Locate white blood cells.
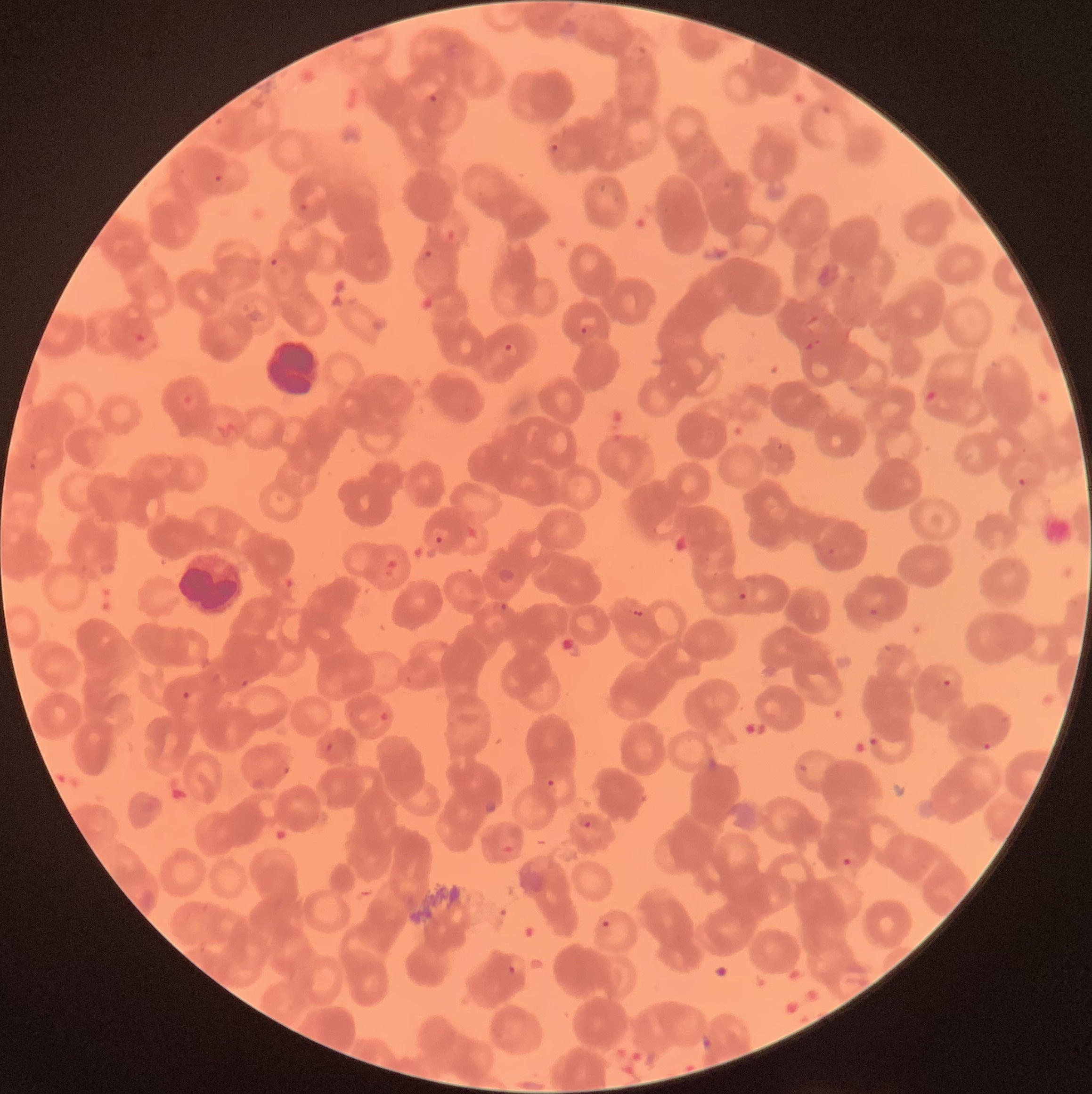
Approximate bounding boxes as named x1/y1/x2/y2 corners in pixels.
White blood cells: (x1=268, y1=337, x2=318, y2=396), (x1=180, y1=552, x2=242, y2=612).

Summary:
  - Plasmodium parasite locations: (x1=425, y1=93, x2=438, y2=103), (x1=549, y1=142, x2=562, y2=160), (x1=214, y1=174, x2=223, y2=182), (x1=298, y1=203, x2=309, y2=214), (x1=423, y1=249, x2=434, y2=258), (x1=269, y1=258, x2=278, y2=266), (x1=581, y1=326, x2=589, y2=335), (x1=504, y1=341, x2=519, y2=355), (x1=30, y1=453, x2=38, y2=472), (x1=1018, y1=478, x2=1026, y2=486), (x1=431, y1=526, x2=449, y2=544), (x1=826, y1=548, x2=835, y2=555), (x1=737, y1=592, x2=748, y2=601), (x1=493, y1=602, x2=509, y2=615), (x1=868, y1=608, x2=879, y2=617), (x1=882, y1=643, x2=892, y2=653), (x1=940, y1=678, x2=952, y2=689), (x1=868, y1=737, x2=878, y2=747), (x1=982, y1=742, x2=992, y2=749), (x1=797, y1=763, x2=808, y2=773), (x1=547, y1=779, x2=555, y2=788), (x1=484, y1=802, x2=497, y2=814), (x1=576, y1=812, x2=596, y2=828), (x1=841, y1=857, x2=852, y2=866), (x1=601, y1=920, x2=610, y2=928), (x1=505, y1=964, x2=519, y2=974)
  - Preparation: thin blood film
  - Red blood cell morphology: rouleaux formation
  - Modality: light microscopy
  - Image size: 1092×1094 pixels